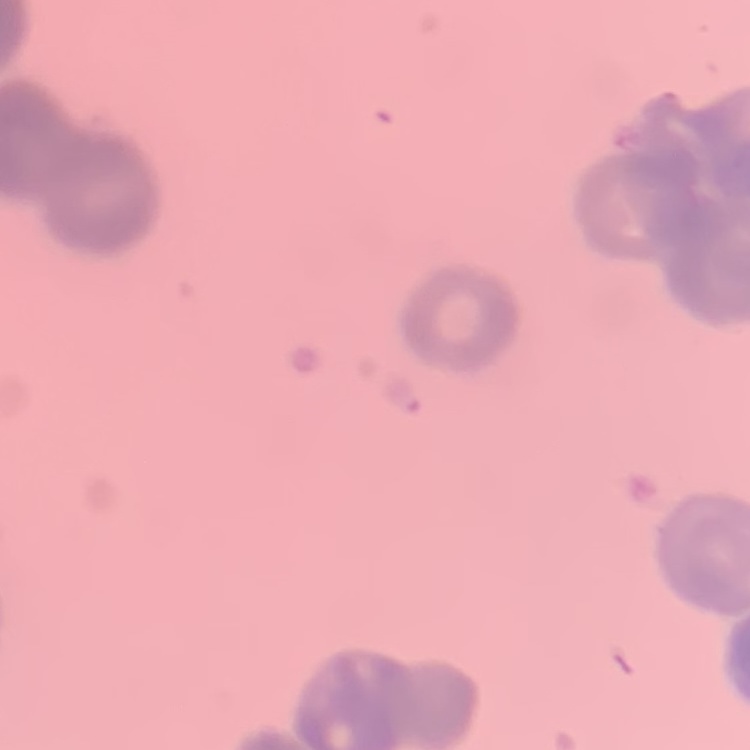 The erythrocytes exhibit rouleaux formation. Thin peripheral smear. Field's or Giemsa stain. One tile cut from a larger photomicrograph.